Report the malaria status of this cell.
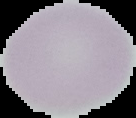
It is uninfected.

From a thin blood smear. Image is 136×118 pixels. The area outside the segmented cell region is set to black.